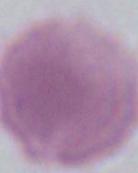

Summary:
  - Magnification: 1000x
  - Modality: micrograph
  - Identification: erythrocyte